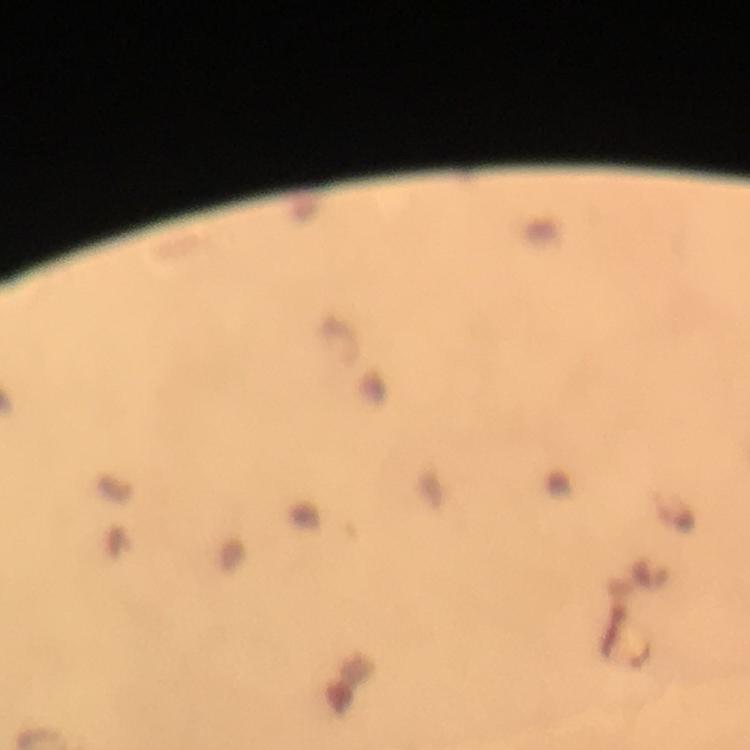
Approximate centers as [x, y] in pixels. Plasmodium parasite locations: [676, 512]. Photographed with a smartphone mounted on the microscope. A crop from one field of view. Immersion oil was used. Image is 750×750 pixels. From a malaria diagnostic workup. 100x magnification. Thick smear. Giemsa-stained preparation.